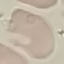 Malaria status: uninfected. Giemsa-stained preparation. Photographed with a smartphone camera at the microscope eyepiece. Cell patch, automatically extracted from a larger field of view and resized to 64 × 64 pixels. Thin blood smear.